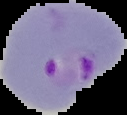
Image is 127×115 pixels. Result: malaria parasites detected. The area outside the segmented cell region is set to black. From a thin blood film.